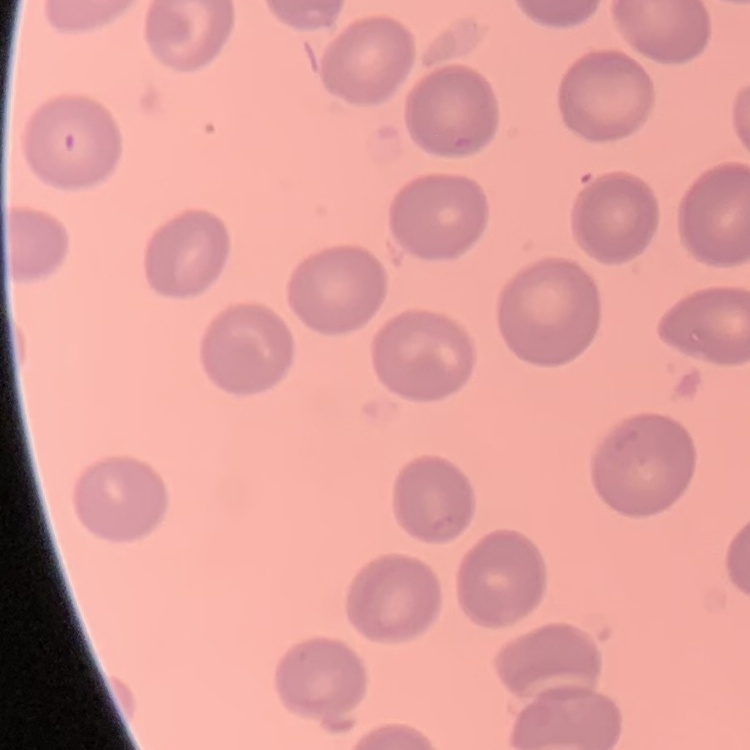

red blood cell morphology = no rouleaux formation
stain = Field's or Giemsa
preparation = thin blood smear
image type = one tile cut from a larger photomicrograph